Report the malaria status of this cell.
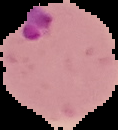

It is parasitized.

preparation = thin blood smear
image size = 118×130 pixels
image type = cell region segmented out of the field of view; surrounding area masked to black